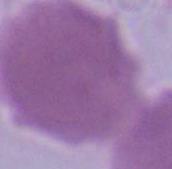

identification = red blood cell
modality = photomicrograph
magnification = 1000x